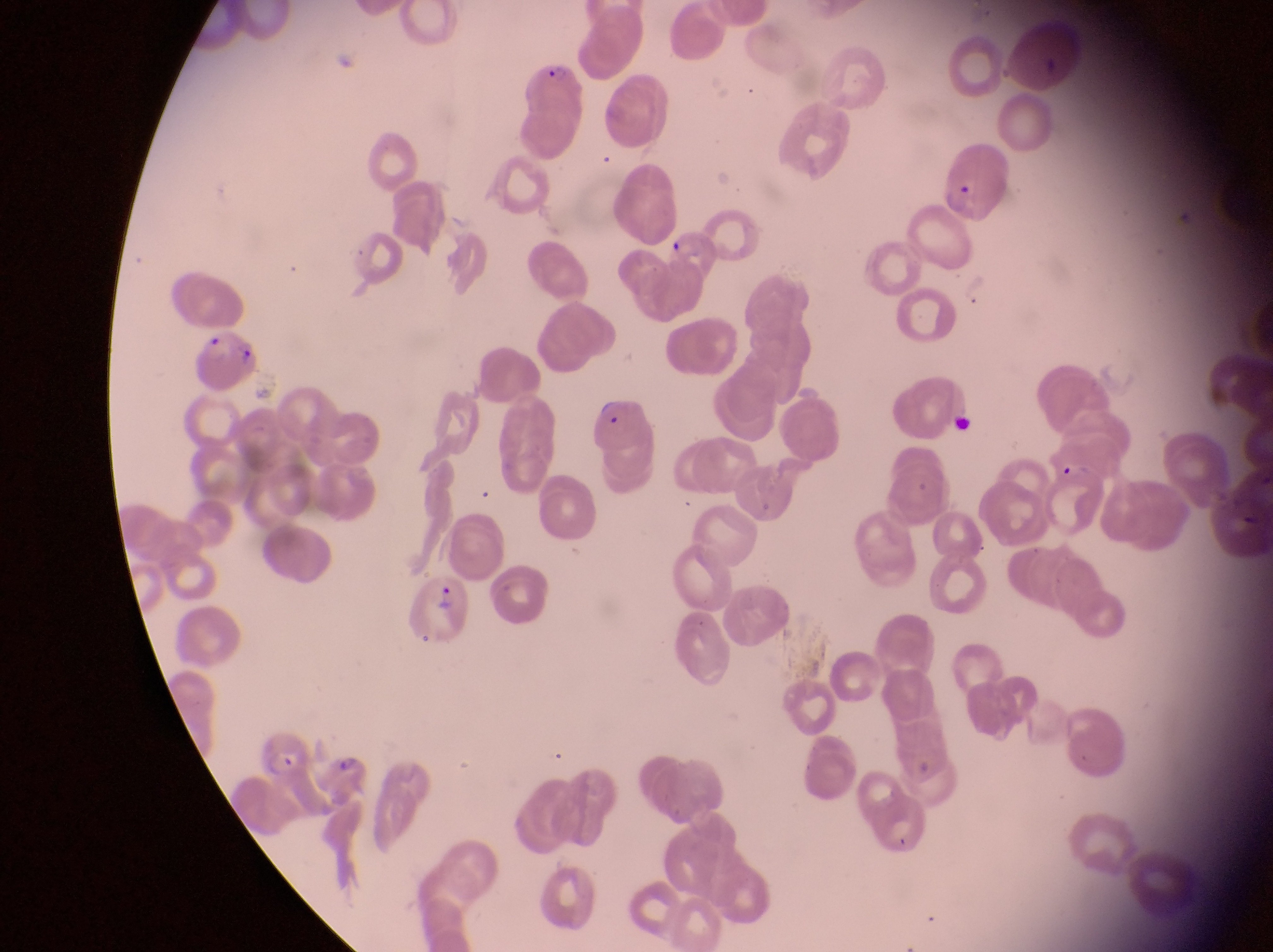

{
  "magnification": "1000x",
  "image_size": "1273×952 pixels",
  "country": "Uganda",
  "capture": "smartphone photograph through the eyepiece of an Olympus CX-23 microscope",
  "parasitised_red_blood_cell_locations": "approximate bounding boxes as left top right bottom in pixels: 523 56 580 148; 934 142 1017 224; 666 229 721 277; 192 332 261 395; 591 390 654 455; 409 575 474 642; 248 727 313 784",
  "preparation": "thin blood film",
  "field_of_view": "single"
}